Identify the parasite.
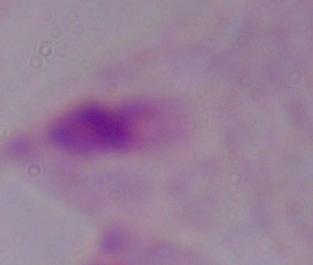
This is a trichomonad.

Captured at 1000x magnification. Micrograph.